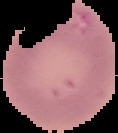
preparation = thin blood film
result = no Plasmodium parasites seen
image type = cell region segmented out of the field of view; surrounding area masked to black
image size = 118×133 pixels